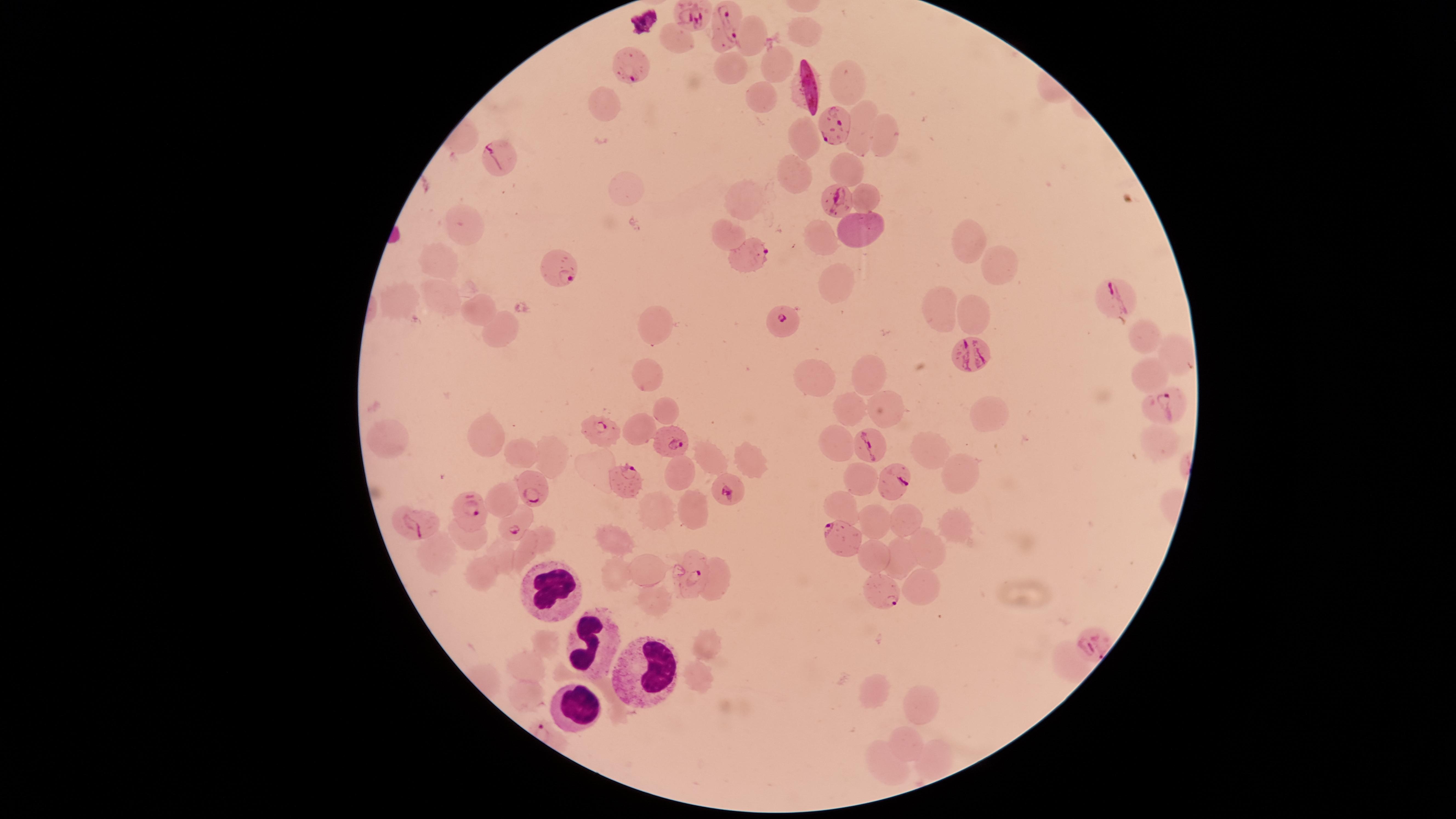

uninfected red blood cells = approximate marker points as [x, y] in pixels: [807, 30], [752, 34], [676, 40], [774, 65], [726, 72], [846, 78], [762, 100], [606, 105], [859, 130], [887, 136], [800, 137], [793, 170], [848, 171], [622, 186], [748, 193], [870, 199], [463, 224], [863, 228], [726, 235], [827, 239], [967, 241], [437, 264], [996, 269], [835, 291], [401, 298], [443, 300], [481, 310], [937, 312], [972, 322], [657, 329], [1143, 329], [499, 333], [1173, 358], [872, 372], [648, 377], [817, 377], [1146, 381], [891, 403], [849, 406], [987, 408], [665, 409], [488, 431], [390, 435], [837, 441], [520, 451], [924, 454], [552, 455], [708, 459], [750, 462], [679, 470], [954, 471], [857, 480], [502, 500], [835, 506], [691, 507], [654, 509], [876, 517], [905, 520], [951, 528], [619, 536], [546, 540], [924, 548], [431, 552], [524, 554], [902, 554], [874, 556], [499, 557], [650, 567], [483, 572], [613, 572], [714, 581], [921, 588], [657, 600], [546, 645], [707, 650], [1069, 661], [527, 663], [697, 672], [871, 689], [521, 697], [924, 702], [904, 740], [879, 754], [937, 754]
parasitized red blood cells = approximate marker points as [x, y] in pixels: [686, 15], [722, 21], [625, 65], [833, 125], [493, 150], [836, 199], [749, 256], [559, 268], [1117, 294], [782, 322], [970, 356], [1167, 402], [601, 428], [676, 440], [872, 443], [628, 478], [892, 483], [530, 487], [726, 490], [470, 505], [410, 519], [515, 521], [837, 537], [692, 574], [880, 591], [1093, 640]
species = Plasmodium falciparum
preparation = thin blood film
presence = malaria parasites identified
image size = 1456×819 pixels
capture = smartphone photograph through the microscope eyepiece
field of view = single
visible region = circular
white blood cells = approximate marker points as [x, y] in pixels: [551, 586], [585, 639], [646, 667], [571, 707]
stain = Giemsa